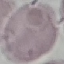
Malaria status: uninfected. Giemsa stain. Acquired by smartphone through the microscope eyepiece. Automatically extracted cell patch, resized to 64 × 64 pixels. Thin blood smear.